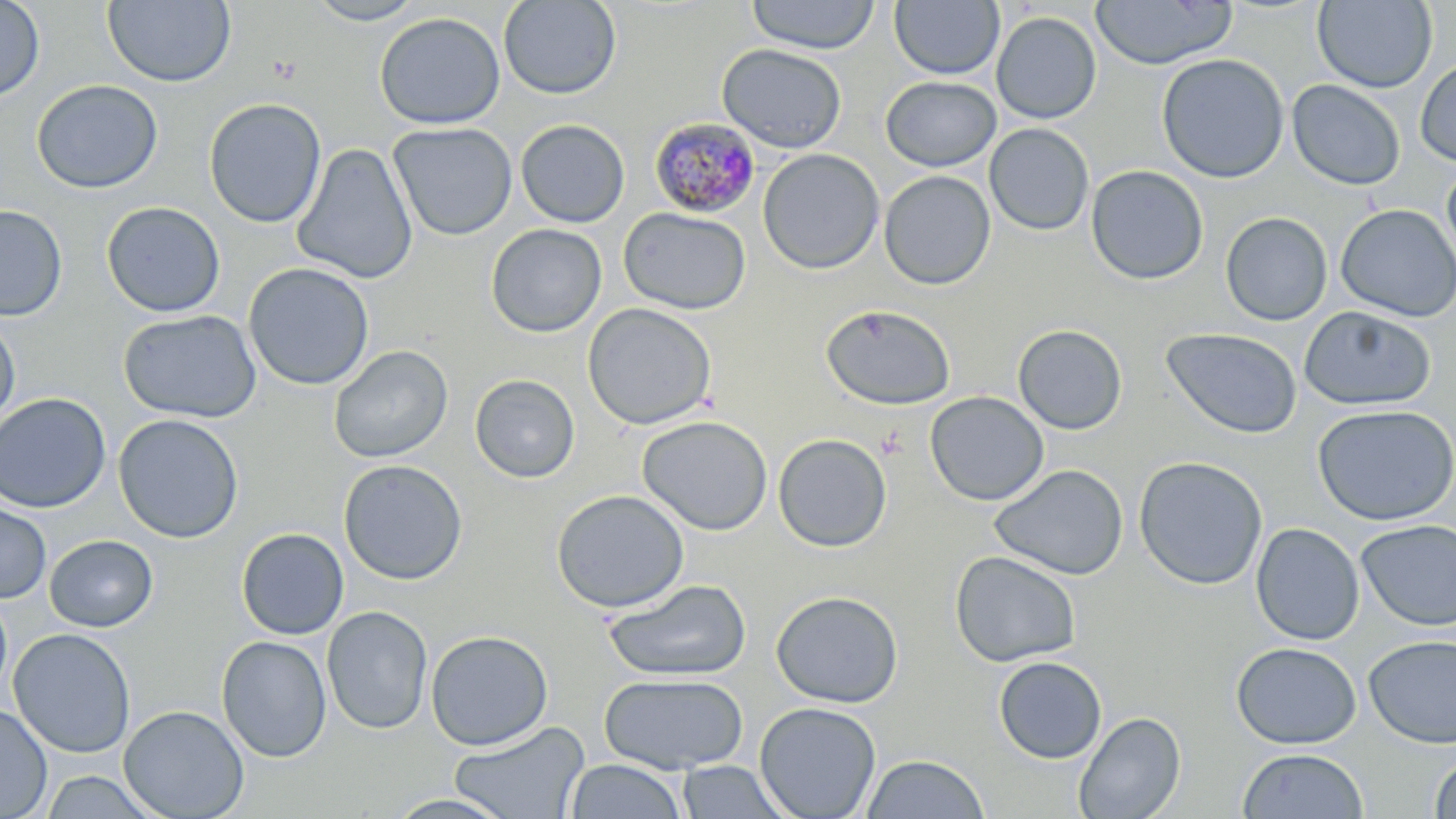

slide-level diagnosis = Plasmodium malariae
field of view = single
preparation = thin blood film
stain = May-Grünwald-Giemsa
magnification = 1000x
modality = light microscopy
uninfected red blood cell locations = approximate bounding boxes as (x1, y1, x2, y2) in pixels: (0, 0, 45, 103), (102, 0, 236, 87), (303, 0, 428, 26), (499, 0, 621, 100), (745, 0, 880, 54), (1091, 0, 1237, 69), (1312, 0, 1437, 92), (889, 1, 1004, 80), (373, 12, 506, 130), (991, 12, 1101, 124), (717, 43, 847, 154), (1156, 53, 1289, 183), (1415, 57, 1456, 167), (881, 76, 1002, 172), (31, 79, 163, 194), (1287, 79, 1405, 191), (204, 97, 327, 228), (515, 119, 629, 228), (388, 122, 518, 241), (984, 123, 1094, 236), (291, 143, 419, 285), (758, 148, 884, 275), (1441, 163, 1456, 275), (1086, 164, 1209, 286), (879, 170, 996, 290), (101, 201, 226, 318), (1335, 204, 1456, 322), (0, 205, 67, 321), (618, 207, 751, 315), (1220, 211, 1333, 326), (486, 224, 607, 338), (243, 262, 375, 391), (582, 303, 717, 431), (821, 304, 956, 411), (1298, 305, 1436, 411), (118, 309, 262, 423), (0, 313, 21, 431), (1012, 324, 1128, 435), (1162, 327, 1302, 439), (328, 345, 453, 463), (470, 374, 580, 483), (925, 391, 1049, 506), (0, 392, 112, 513), (2, 402, 244, 520), (1312, 405, 1456, 526), (113, 414, 244, 543), (637, 415, 773, 535), (773, 433, 892, 552), (1133, 455, 1269, 590), (338, 459, 468, 585), (989, 463, 1129, 581), (551, 489, 690, 613), (0, 497, 51, 604), (1356, 519, 1456, 631), (1250, 523, 1364, 645), (236, 528, 349, 640), (44, 534, 158, 632), (949, 550, 1082, 667), (603, 578, 752, 682), (771, 589, 904, 707), (0, 591, 13, 702), (321, 606, 433, 735), (9, 628, 136, 758), (426, 629, 553, 750), (1363, 634, 1456, 748), (216, 635, 332, 763), (1231, 642, 1361, 749), (993, 656, 1107, 764), (598, 673, 749, 774), (754, 701, 882, 819), (0, 703, 53, 819), (118, 705, 250, 818), (1073, 711, 1186, 819), (448, 720, 590, 819), (1236, 748, 1369, 819), (1428, 753, 1456, 818), (859, 754, 990, 818), (563, 759, 689, 818), (675, 760, 794, 818), (40, 770, 161, 818), (383, 792, 517, 818)
image size = 1456×819 pixels
Plasmodium malariae-infected red blood cell locations = approximate bounding boxes as (x1, y1, x2, y2) in pixels: (649, 118, 761, 219)